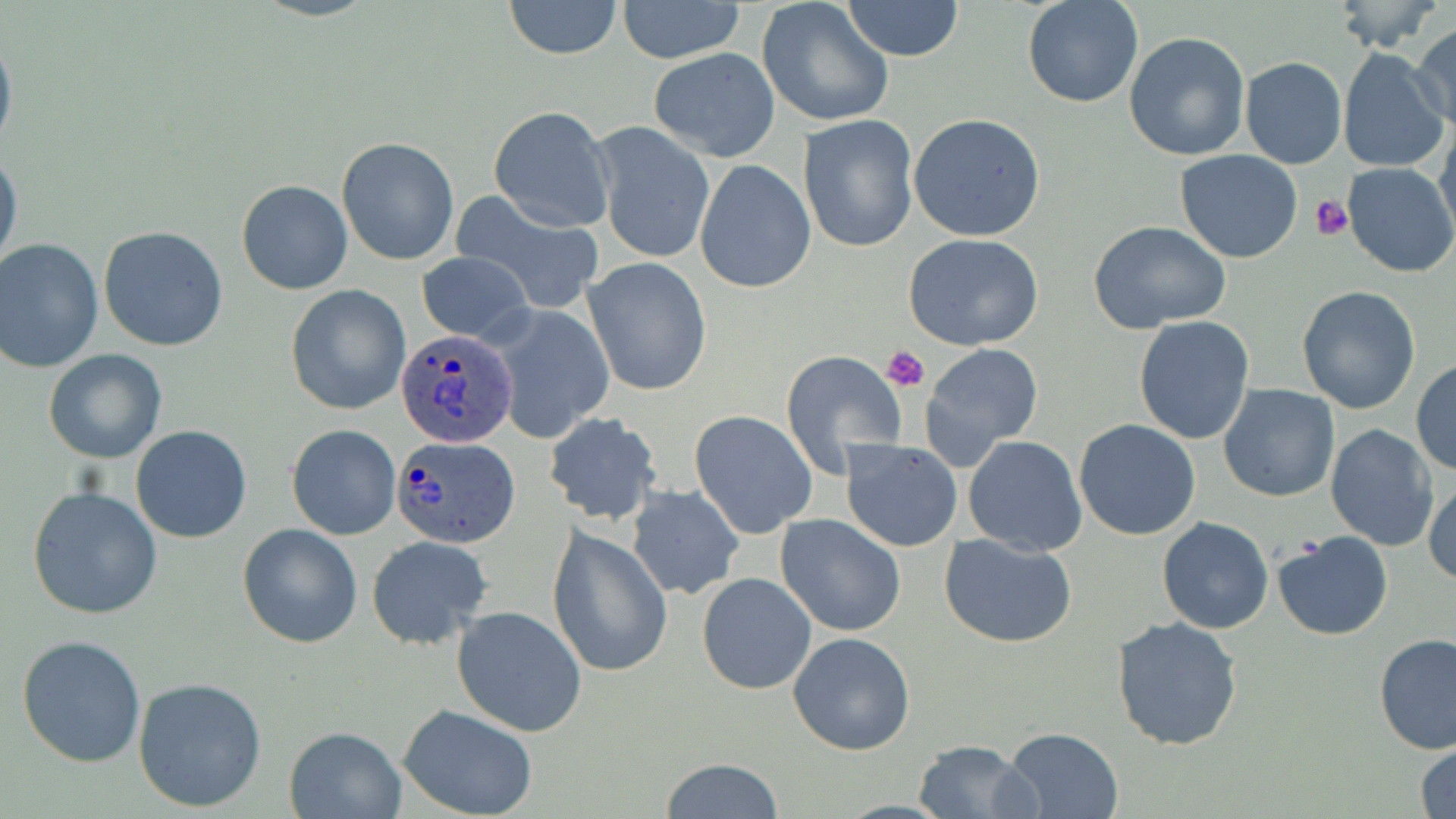

slide-level diagnosis = Plasmodium ovale
magnification = 1000x
modality = light microscopy
Plasmodium ovale-infected red blood cell locations = approximate bounding boxes as named x1/y1/x2/y2 corners in pixels: (x1=394, y1=329, x2=517, y2=449), (x1=391, y1=436, x2=518, y2=549)
stain = May-Grünwald-Giemsa
preparation = thin blood film
field of view = single
image size = 1456×819 pixels
uninfected red blood cell locations = approximate bounding boxes as named x1/y1/x2/y2 corners in pixels: (x1=501, y1=0, x2=625, y2=58), (x1=616, y1=0, x2=745, y2=63), (x1=758, y1=0, x2=895, y2=128), (x1=1022, y1=0, x2=1143, y2=109), (x1=839, y1=1, x2=965, y2=61), (x1=1331, y1=1, x2=1443, y2=53), (x1=0, y1=25, x2=17, y2=163), (x1=1411, y1=25, x2=1455, y2=131), (x1=1125, y1=31, x2=1252, y2=162), (x1=1337, y1=47, x2=1448, y2=175), (x1=648, y1=48, x2=781, y2=161), (x1=1239, y1=57, x2=1348, y2=170), (x1=488, y1=106, x2=614, y2=232), (x1=908, y1=113, x2=1046, y2=242), (x1=799, y1=114, x2=919, y2=253), (x1=1436, y1=116, x2=1456, y2=243), (x1=592, y1=125, x2=715, y2=265), (x1=336, y1=136, x2=459, y2=266), (x1=1174, y1=148, x2=1303, y2=264), (x1=0, y1=149, x2=23, y2=274), (x1=694, y1=159, x2=816, y2=294), (x1=1341, y1=164, x2=1456, y2=278), (x1=236, y1=179, x2=352, y2=295), (x1=453, y1=192, x2=606, y2=313), (x1=1089, y1=221, x2=1232, y2=334), (x1=99, y1=225, x2=230, y2=352), (x1=903, y1=235, x2=1046, y2=352), (x1=0, y1=238, x2=104, y2=373), (x1=417, y1=251, x2=533, y2=345), (x1=583, y1=257, x2=713, y2=396), (x1=286, y1=285, x2=412, y2=415), (x1=1297, y1=286, x2=1420, y2=413), (x1=488, y1=306, x2=613, y2=443), (x1=1133, y1=316, x2=1255, y2=444), (x1=918, y1=342, x2=1045, y2=471), (x1=43, y1=349, x2=167, y2=464), (x1=780, y1=349, x2=907, y2=475), (x1=1411, y1=358, x2=1456, y2=476), (x1=1218, y1=382, x2=1341, y2=503), (x1=544, y1=412, x2=663, y2=525), (x1=689, y1=412, x2=817, y2=538), (x1=1074, y1=418, x2=1201, y2=540), (x1=1324, y1=423, x2=1438, y2=551), (x1=287, y1=424, x2=400, y2=539), (x1=130, y1=426, x2=253, y2=544), (x1=964, y1=436, x2=1088, y2=556), (x1=841, y1=440, x2=963, y2=551), (x1=1424, y1=473, x2=1456, y2=587), (x1=626, y1=484, x2=744, y2=600), (x1=27, y1=485, x2=163, y2=619), (x1=775, y1=515, x2=906, y2=637), (x1=1156, y1=518, x2=1274, y2=635), (x1=237, y1=523, x2=362, y2=648), (x1=547, y1=527, x2=673, y2=677), (x1=1271, y1=531, x2=1393, y2=641), (x1=938, y1=534, x2=1078, y2=647), (x1=367, y1=536, x2=493, y2=650), (x1=697, y1=573, x2=817, y2=694), (x1=451, y1=606, x2=587, y2=736), (x1=1112, y1=617, x2=1243, y2=752), (x1=789, y1=632, x2=914, y2=756), (x1=17, y1=634, x2=148, y2=767), (x1=1372, y1=634, x2=1456, y2=756), (x1=134, y1=676, x2=268, y2=812), (x1=398, y1=705, x2=539, y2=818), (x1=285, y1=726, x2=405, y2=818), (x1=1000, y1=727, x2=1124, y2=818), (x1=911, y1=738, x2=1034, y2=818), (x1=1414, y1=743, x2=1456, y2=819), (x1=660, y1=757, x2=786, y2=817)
platelet locations = approximate bounding boxes as named x1/y1/x2/y2 corners in pixels: (x1=1311, y1=195, x2=1353, y2=241), (x1=882, y1=346, x2=929, y2=392)